Classify this cell by malaria status.
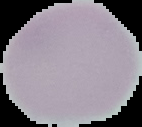

Uninfected.

Summary:
  - Image type: cell region segmented out of the field of view; surrounding area masked to black
  - Preparation: thin blood smear
  - Image size: 142×127 pixels